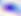
Micrograph. Toxoplasma gondii is seen. 400x magnification.